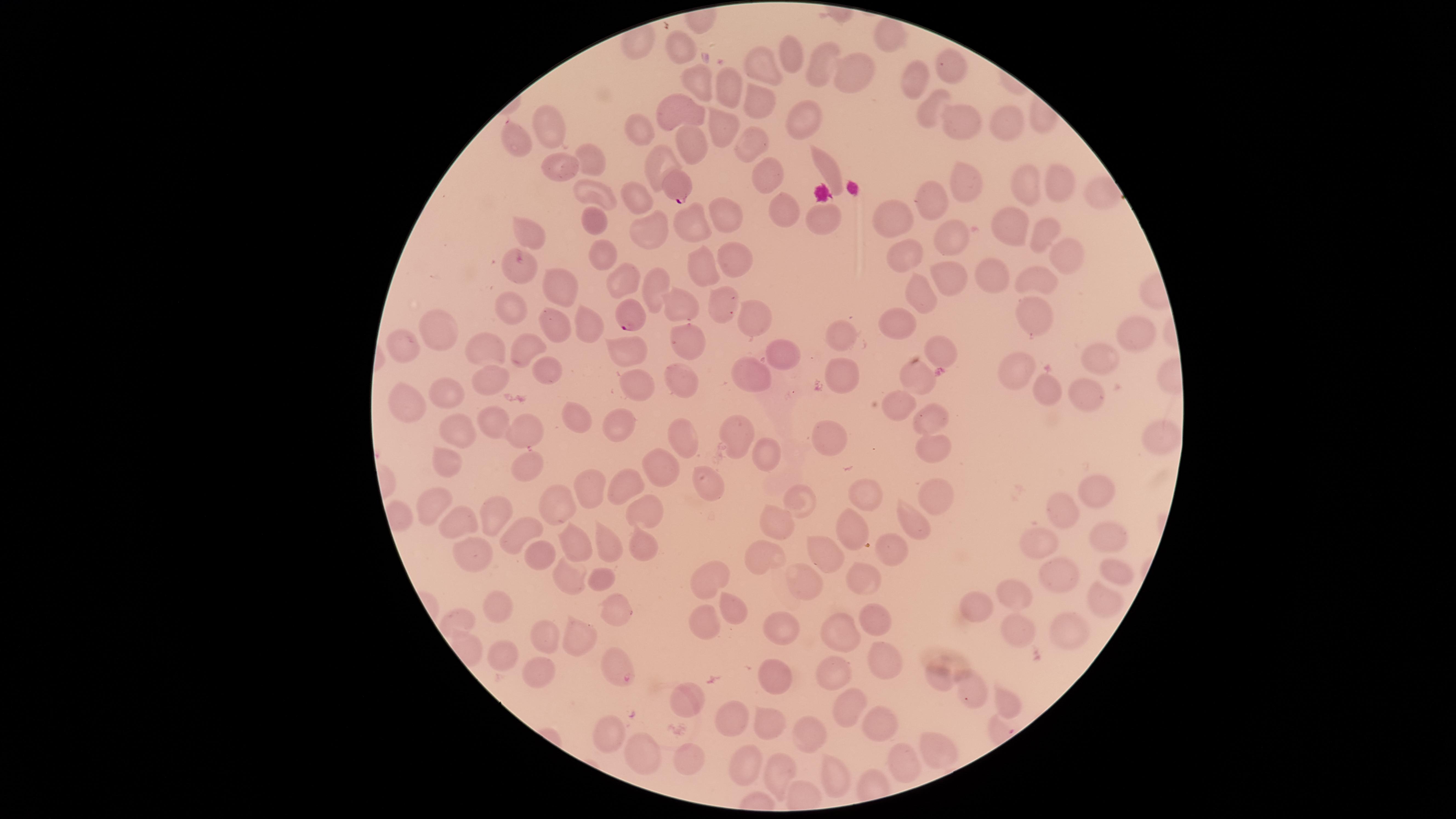

Approximate marker points as [x, y] in pixels.
Summary:
  - Uninfected RBCs: [886, 33], [683, 47], [786, 59], [760, 64], [820, 65], [945, 65], [920, 79], [854, 80], [702, 82], [730, 87], [760, 94], [684, 104], [934, 108], [803, 118], [720, 122], [967, 122], [1006, 126], [551, 128], [640, 128], [749, 138], [515, 141], [691, 142], [590, 162], [659, 163], [824, 163], [552, 166], [770, 174], [1057, 182], [1029, 185], [959, 187], [631, 188], [590, 190], [1101, 190], [931, 204], [785, 208], [719, 216], [826, 218], [897, 219], [597, 226], [1010, 229], [642, 230], [690, 230], [1041, 232], [943, 233], [529, 237], [602, 255], [903, 256], [1058, 257], [730, 258], [700, 270], [519, 272], [951, 274], [990, 275], [623, 280], [654, 282], [1033, 282], [563, 285], [926, 291], [722, 303], [516, 308], [684, 309], [1034, 317], [752, 318], [898, 320], [550, 322], [589, 331], [1135, 331], [440, 333], [837, 336], [400, 345], [517, 345], [687, 345], [484, 346], [624, 347], [939, 348], [1099, 349], [778, 350], [542, 371], [923, 373], [1015, 373], [752, 374], [846, 378], [636, 381], [681, 381], [1045, 381], [487, 382], [1080, 392], [409, 393], [450, 396], [896, 409], [935, 413], [569, 417], [527, 421], [623, 425], [457, 427], [497, 427], [738, 429], [1157, 433], [832, 439], [680, 441], [929, 450], [776, 454], [448, 456], [523, 464], [661, 469], [699, 483], [628, 484], [590, 486], [938, 488], [795, 496], [869, 499], [1095, 500], [436, 504], [561, 505], [646, 512], [1066, 515], [498, 516], [461, 521], [770, 526], [906, 526], [524, 529], [851, 531], [1111, 531], [1045, 541], [602, 543], [642, 546], [577, 549], [536, 550], [471, 554], [760, 554], [887, 554], [825, 562], [1110, 569], [569, 576], [600, 577], [864, 578], [1061, 578], [711, 579], [802, 585], [1104, 599], [495, 600], [1020, 602], [615, 610], [736, 613], [979, 613], [699, 622], [875, 622], [784, 623], [1068, 629], [843, 631], [580, 632], [1015, 634], [543, 635], [875, 654], [505, 657], [531, 671], [617, 672], [833, 676], [936, 676], [776, 683], [970, 692], [1005, 697], [688, 705], [848, 709], [725, 715], [767, 722], [869, 726], [609, 731], [808, 735], [935, 749], [688, 759], [646, 760], [902, 760], [748, 762], [777, 776], [828, 776]
  - Parasitized RBCs: [679, 183], [628, 313]
  - Field of view: single
  - Visible region: circular
  - Preparation: thin blood smear
  - Capture: smartphone photograph through the microscope eyepiece
  - Species: Plasmodium falciparum
  - Presence: malaria parasites identified
  - Stain: Giemsa
  - Image size: 1456×819 pixels